Name the cell type shown.
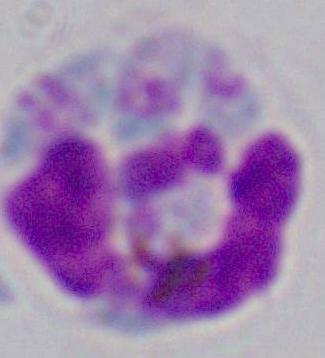

A leukocyte.

Captured at 1000x magnification. Photomicrograph.